Locate and identify every blood parasite.
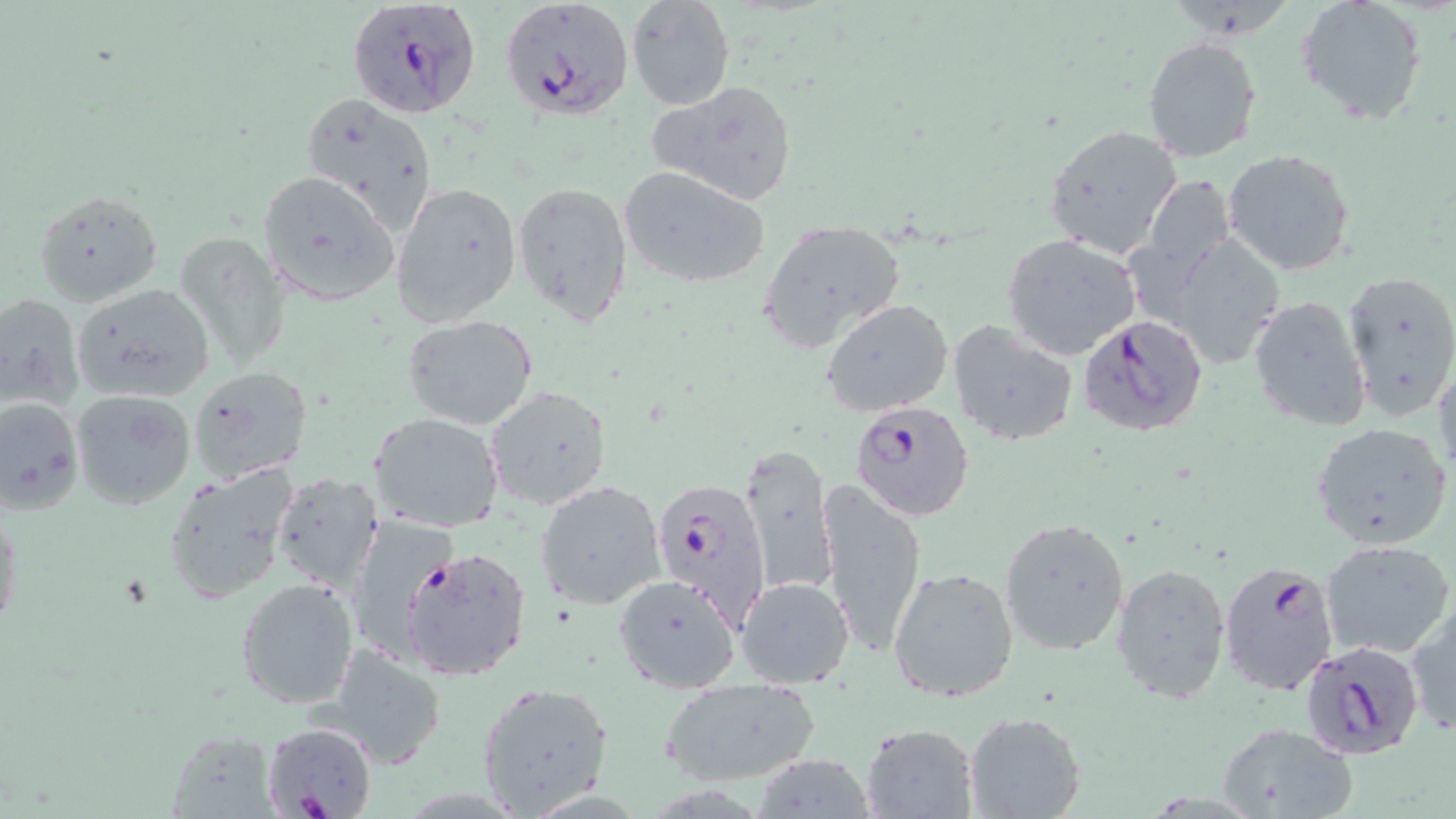

Approximate bounding boxes as [x1, y1, x2, y2] in pixels.
Plasmodium falciparum-infected red blood cells (subset): [349, 1, 479, 118], [1077, 314, 1208, 439], [850, 398, 974, 521], [649, 478, 772, 628], [399, 546, 531, 680], [1218, 561, 1339, 696], [1308, 642, 1422, 760], [261, 721, 379, 819].
No Plasmodium ovale, Plasmodium malariae, Plasmodium vivax, Babesia divergens, or Trypanosoma brucei observed.

Summary:
  - Uninfected red blood cell locations (subset): [627, 0, 733, 111], [1168, 0, 1291, 43], [1297, 0, 1426, 123], [1142, 36, 1262, 163], [649, 80, 799, 206], [301, 94, 436, 231], [1042, 123, 1185, 260], [1222, 148, 1356, 275], [616, 165, 770, 289], [259, 169, 400, 306], [1136, 172, 1232, 311], [392, 180, 523, 331], [512, 180, 633, 325], [32, 189, 162, 307], [757, 217, 907, 352], [176, 229, 293, 374], [1168, 233, 1288, 373], [1002, 234, 1141, 360], [1341, 268, 1456, 419], [72, 283, 216, 403], [0, 290, 83, 408], [1248, 295, 1372, 433], [822, 300, 953, 417], [401, 314, 538, 430], [946, 320, 1078, 446], [1433, 353, 1455, 488], [186, 364, 312, 485], [484, 385, 612, 509], [70, 389, 196, 509], [0, 394, 83, 515], [369, 412, 505, 534], [1311, 420, 1452, 550], [738, 442, 836, 596], [159, 461, 299, 602], [270, 472, 384, 592], [536, 480, 668, 612], [817, 481, 929, 657], [0, 503, 22, 638], [347, 513, 460, 658], [999, 516, 1130, 655], [1322, 538, 1455, 658], [1112, 562, 1231, 703], [888, 566, 1020, 701], [613, 574, 742, 694], [235, 576, 359, 708], [735, 576, 854, 688], [1405, 602, 1456, 739], [321, 643, 448, 769], [658, 678, 822, 786], [474, 680, 615, 817], [964, 710, 1087, 818], [861, 723, 978, 817], [1216, 723, 1358, 818], [164, 730, 281, 817], [756, 754, 877, 819]
  - Slide-level diagnosis: Plasmodium falciparum
  - Magnification: 1000x
  - Field of view: one of a larger specimen
  - Modality: light microscopy
  - Image size: 1456×819 pixels
  - Stain: May-Grünwald-Giemsa
  - Preparation: thin blood smear